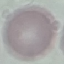
Result: no malaria parasites detected. Thin blood film. Automatically extracted cell patch, resized to 64 × 64 pixels. Giemsa-stained preparation. Photographed with a smartphone camera at the microscope eyepiece.